Assess the morphology of the red blood cells.
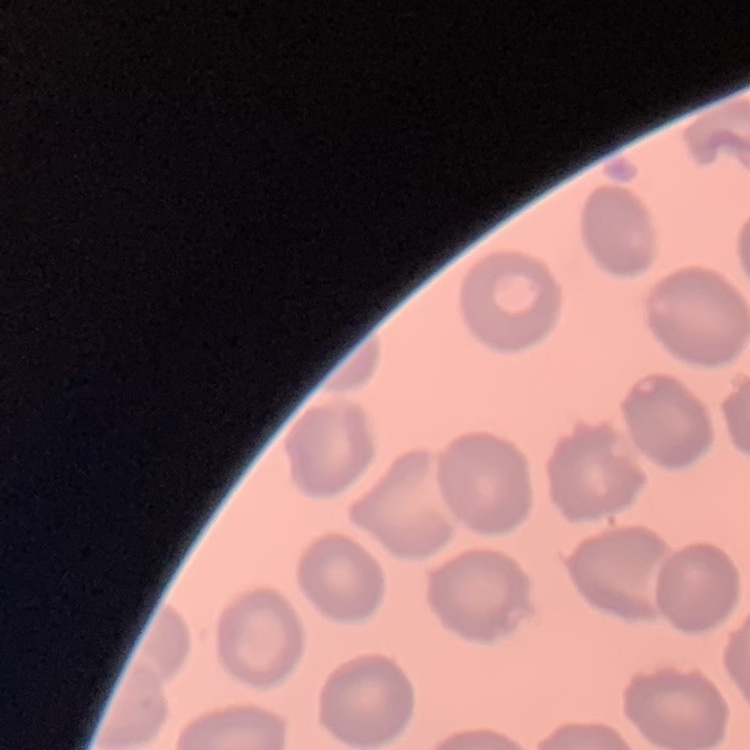

They show no rouleaux formation.

Summary:
  - Image type: square crop of a larger photomicrograph
  - Stain: Field's or Giemsa
  - Preparation: thin blood film